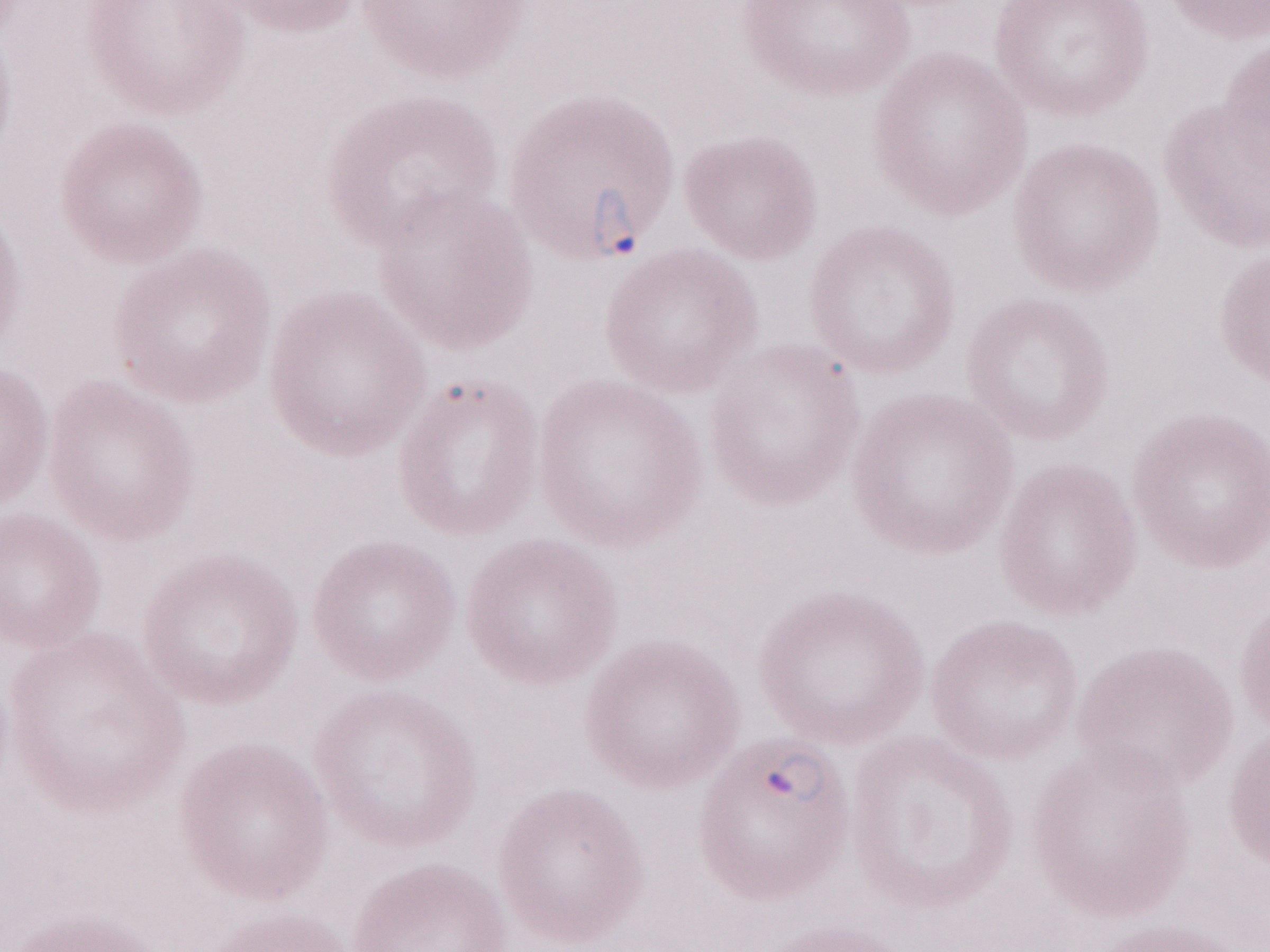

Olympus BX43 microscope, Olympus DP73 camera. One field of this slide. Magnification: 1,000x. Thin blood smear. Patient diagnosis: malaria infection. Image is 1270×952 pixels. May-Grünwald-Giemsa-stained preparation.